Assess the morphology of the erythrocytes.
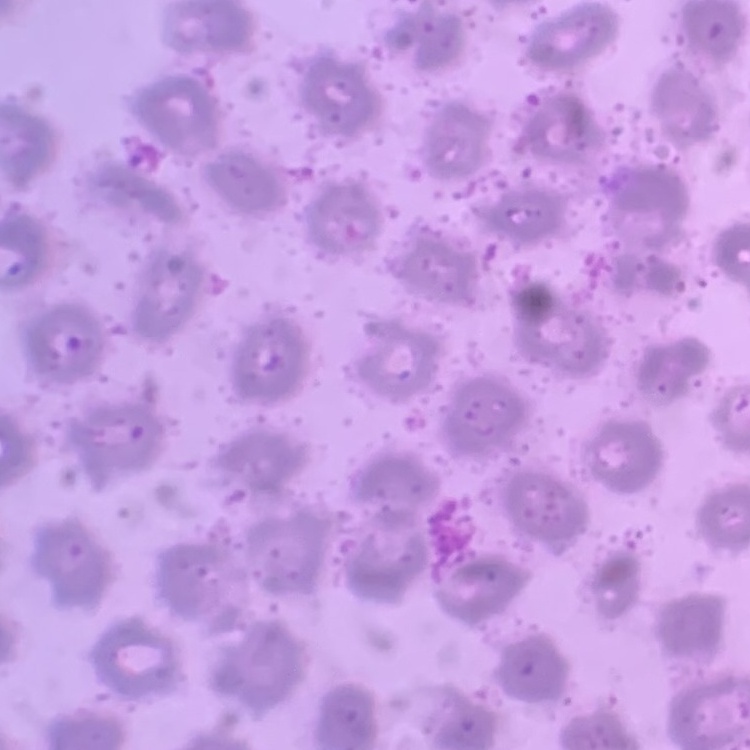
No rouleaux formation.

Field's or Giemsa stain. Thin blood smear. Square crop of a larger photomicrograph.